Classify this cell by malaria status.
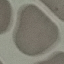

It is uninfected.

preparation = thin blood smear
image type = cell patch, automatically extracted from a larger field of view and resized to 64 × 64 pixels
capture = smartphone through the microscope eyepiece
stain = Giemsa